Identify the parasite.
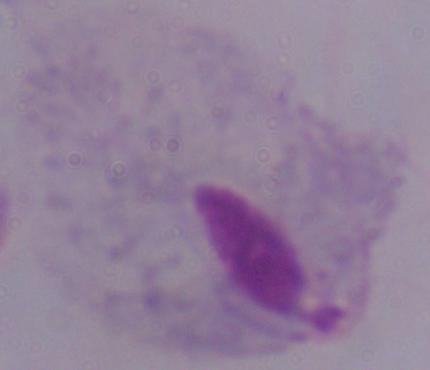
A trichomonad.

1000x magnification. Photomicrograph.